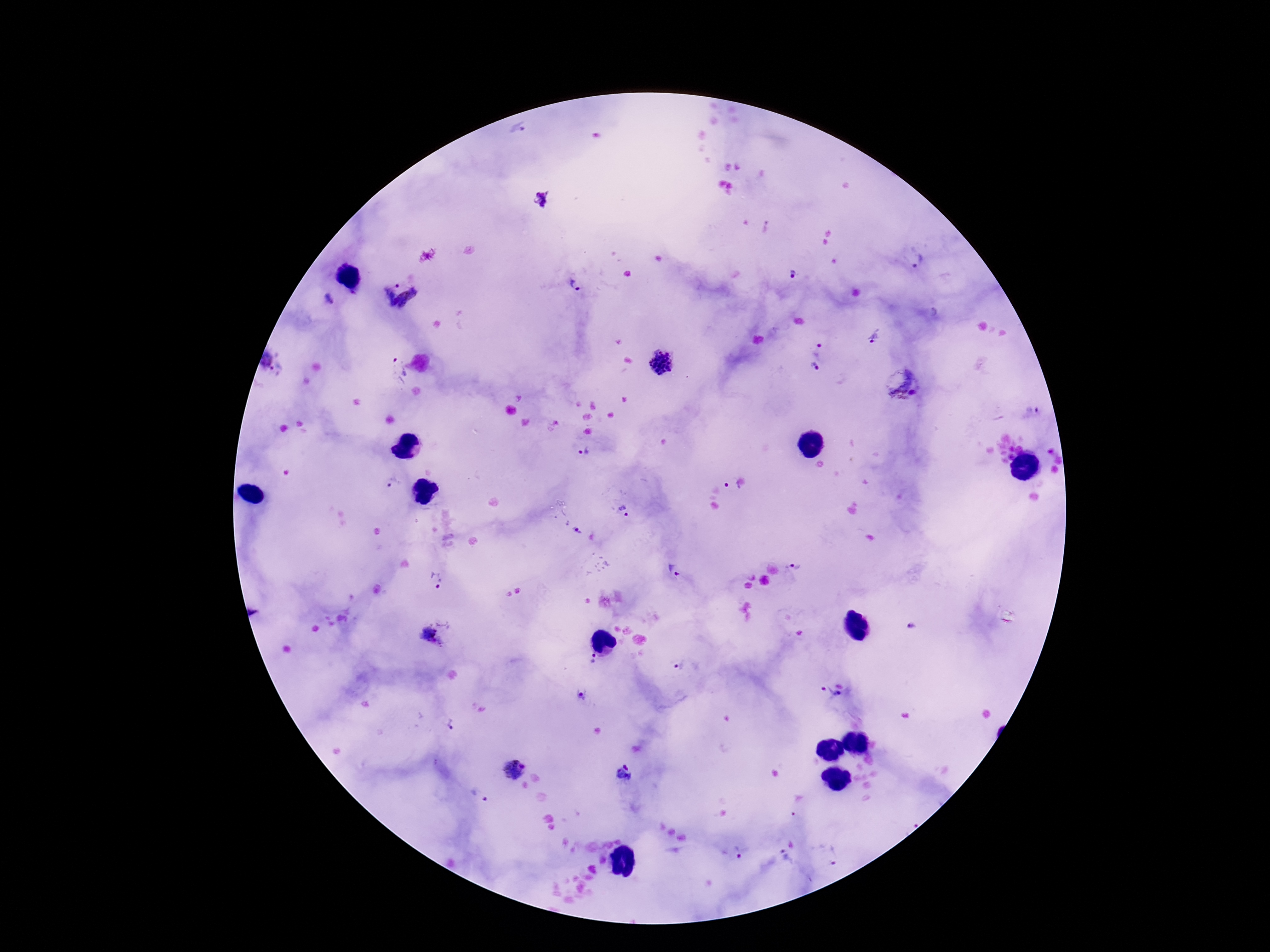
{
  "stain": "Giemsa",
  "plasmodium_parasite_locations": "approximate centers as {x, y} in pixels: {520, 133}, {541, 197}, {919, 261}, {791, 275}, {576, 285}, {399, 297}, {328, 299}, {875, 335}, {820, 348}, {265, 361}, {661, 363}, {814, 368}, {279, 370}, {394, 370}, {902, 385}, {1030, 411}, {585, 452}, {392, 484}, {732, 485}, {624, 512}, {576, 531}, {796, 568}, {673, 571}, {438, 579}, {912, 626}, {432, 638}, {593, 661}, {678, 666}, {827, 692}, {838, 694}, {580, 697}, {451, 724}, {512, 770}, {626, 773}, {479, 796}, {736, 854}, {835, 855}, {785, 861}",
  "magnification": "100x",
  "preparation": "thick blood film",
  "patient_malaria_status": "infected",
  "field_of_view": "one from this slide",
  "image_size": "1270×952 pixels",
  "capture": "smartphone camera through the microscope eyepiece"
}